Classify this cell by malaria status.
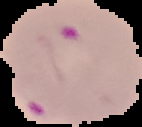

Parasitized.

preparation: thin blood smear
image_size: 142×127 pixels
image_type: segmented cell region with the area outside set to black